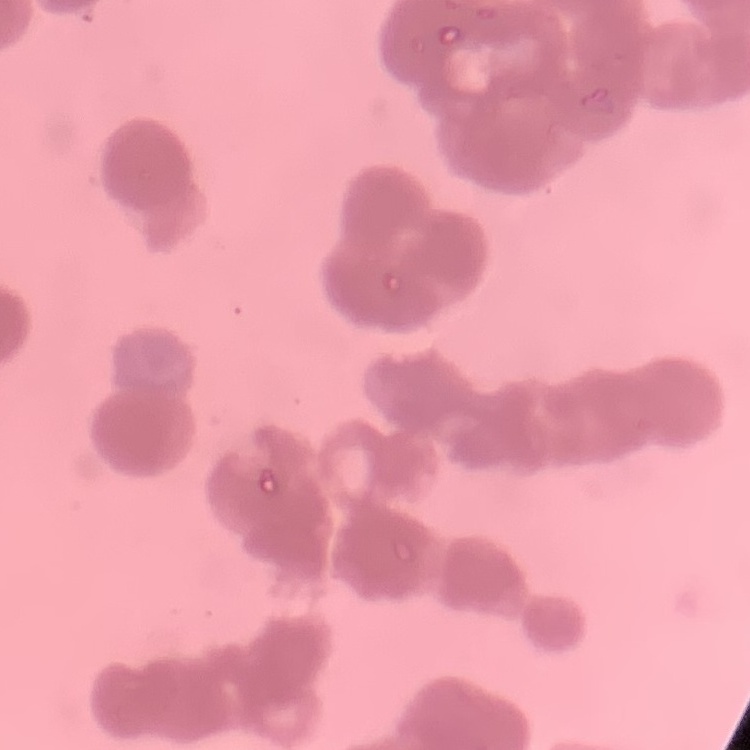

Summary:
  - Red blood cell morphology: rouleaux formation
  - Image type: one tile cut from a larger photomicrograph
  - Stain: Field's or Giemsa
  - Preparation: thin peripheral smear